State the blood parasite species.
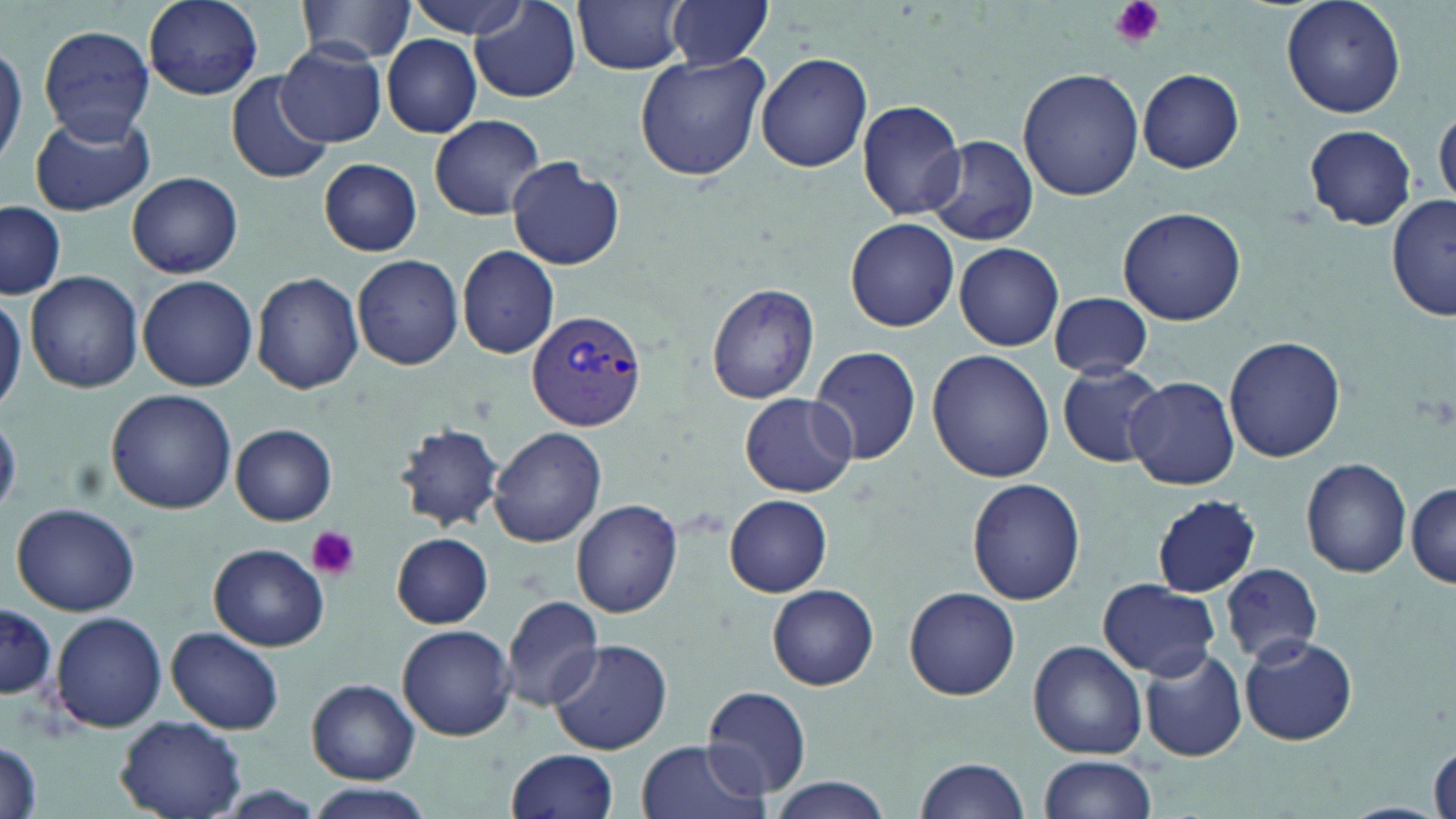

Plasmodium vivax.

preparation = thin blood film
Plasmodium vivax-infected red blood cell locations = approximate bounding boxes as named x1/y1/x2/y2 corners in pixels: (x1=526, y1=307, x2=646, y2=432)
modality = optical microscopy
stain = May-Grünwald-Giemsa
platelet locations = approximate bounding boxes as named x1/y1/x2/y2 corners in pixels: (x1=1109, y1=0, x2=1166, y2=49), (x1=308, y1=526, x2=360, y2=579)
magnification = 1000x
field of view = single
uninfected red blood cell locations = approximate bounding boxes as named x1/y1/x2/y2 corners in pixels: (x1=144, y1=0, x2=264, y2=100), (x1=296, y1=0, x2=416, y2=64), (x1=403, y1=0, x2=530, y2=37), (x1=470, y1=0, x2=580, y2=102), (x1=573, y1=0, x2=691, y2=75), (x1=665, y1=0, x2=774, y2=72), (x1=1282, y1=0, x2=1406, y2=119), (x1=39, y1=25, x2=155, y2=140), (x1=383, y1=36, x2=481, y2=138), (x1=0, y1=41, x2=26, y2=167), (x1=277, y1=41, x2=388, y2=147), (x1=633, y1=52, x2=770, y2=181), (x1=755, y1=52, x2=872, y2=173), (x1=1018, y1=68, x2=1144, y2=201), (x1=1137, y1=68, x2=1245, y2=174), (x1=225, y1=71, x2=333, y2=187), (x1=859, y1=98, x2=969, y2=220), (x1=28, y1=110, x2=154, y2=217), (x1=1435, y1=110, x2=1455, y2=207), (x1=428, y1=114, x2=546, y2=220), (x1=1304, y1=125, x2=1416, y2=231), (x1=925, y1=135, x2=1038, y2=246), (x1=506, y1=156, x2=626, y2=271), (x1=317, y1=157, x2=422, y2=256), (x1=126, y1=172, x2=243, y2=278), (x1=1388, y1=195, x2=1454, y2=322), (x1=0, y1=202, x2=67, y2=299), (x1=1118, y1=206, x2=1246, y2=325), (x1=846, y1=218, x2=960, y2=332), (x1=953, y1=242, x2=1065, y2=351), (x1=456, y1=247, x2=561, y2=358), (x1=351, y1=255, x2=464, y2=369), (x1=24, y1=271, x2=143, y2=392), (x1=252, y1=272, x2=364, y2=393), (x1=136, y1=274, x2=259, y2=391), (x1=706, y1=281, x2=821, y2=405), (x1=0, y1=288, x2=25, y2=414), (x1=1049, y1=291, x2=1153, y2=380), (x1=1224, y1=335, x2=1345, y2=462), (x1=808, y1=346, x2=921, y2=465), (x1=926, y1=350, x2=1055, y2=483), (x1=1056, y1=362, x2=1168, y2=469), (x1=1124, y1=375, x2=1239, y2=491), (x1=106, y1=389, x2=237, y2=515), (x1=738, y1=395, x2=852, y2=496), (x1=394, y1=422, x2=506, y2=531), (x1=231, y1=425, x2=336, y2=524), (x1=488, y1=426, x2=606, y2=547), (x1=1301, y1=456, x2=1411, y2=579), (x1=965, y1=478, x2=1087, y2=607), (x1=1408, y1=481, x2=1456, y2=587), (x1=724, y1=494, x2=833, y2=596), (x1=1150, y1=495, x2=1261, y2=597), (x1=571, y1=499, x2=682, y2=619), (x1=11, y1=503, x2=141, y2=617), (x1=391, y1=532, x2=493, y2=628), (x1=208, y1=543, x2=329, y2=652), (x1=1220, y1=563, x2=1323, y2=665), (x1=1097, y1=580, x2=1221, y2=679), (x1=768, y1=583, x2=878, y2=690), (x1=904, y1=585, x2=1020, y2=700), (x1=499, y1=593, x2=605, y2=711), (x1=0, y1=599, x2=56, y2=703), (x1=53, y1=611, x2=167, y2=732), (x1=397, y1=624, x2=517, y2=741), (x1=167, y1=626, x2=285, y2=734), (x1=1238, y1=635, x2=1358, y2=746), (x1=548, y1=639, x2=673, y2=756), (x1=1027, y1=640, x2=1147, y2=759), (x1=1138, y1=645, x2=1247, y2=762), (x1=306, y1=678, x2=419, y2=783), (x1=701, y1=684, x2=811, y2=799), (x1=115, y1=715, x2=246, y2=819), (x1=1, y1=738, x2=43, y2=819), (x1=635, y1=738, x2=763, y2=819), (x1=1429, y1=741, x2=1455, y2=819), (x1=504, y1=748, x2=618, y2=819), (x1=913, y1=755, x2=1033, y2=818), (x1=1038, y1=755, x2=1159, y2=819), (x1=765, y1=778, x2=891, y2=818), (x1=309, y1=784, x2=437, y2=819)
image size = 1456×819 pixels